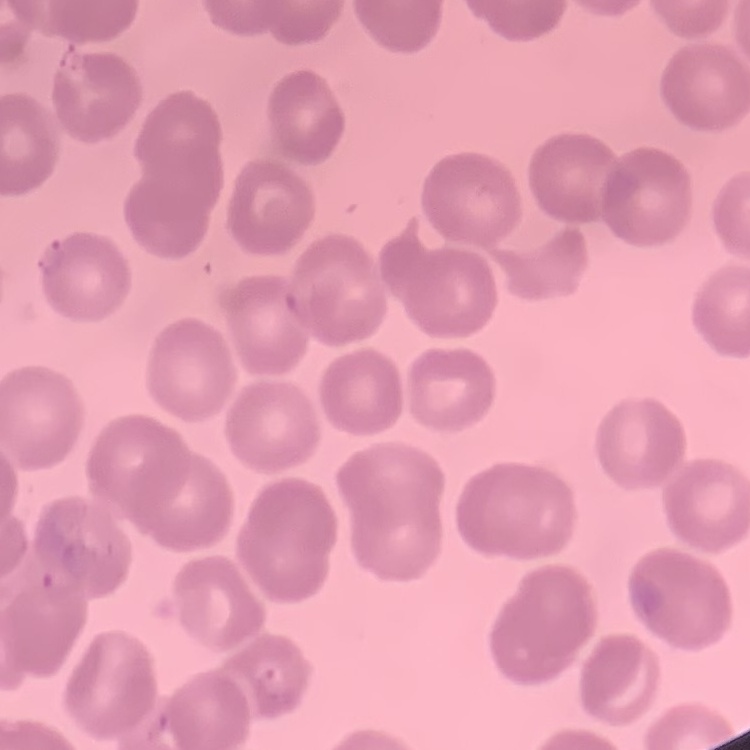 The red blood cells show no rouleaux formation. Stained with either Field's or Giemsa. Thin peripheral smear. One tile cut from a larger photomicrograph.